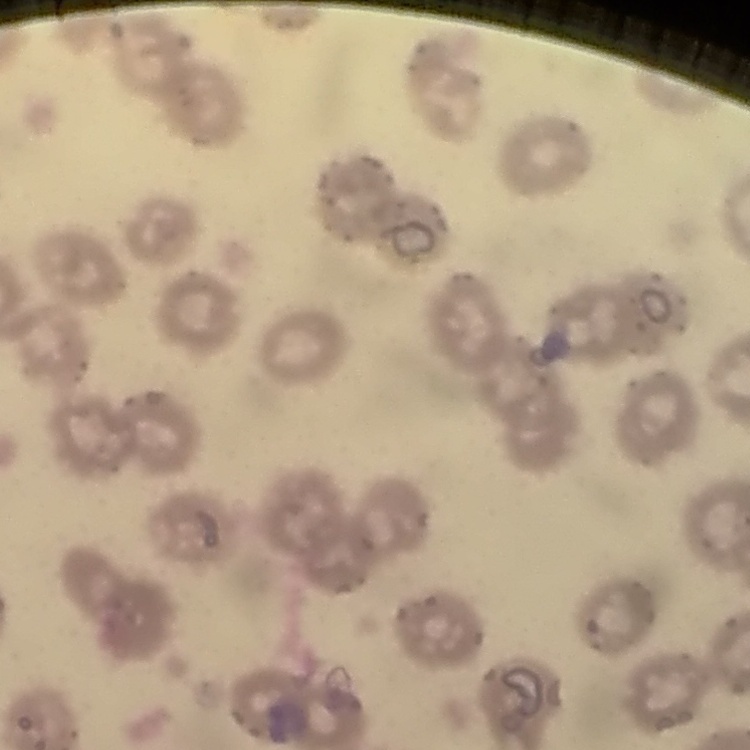 The erythrocytes show no rouleaux formation. Thin blood smear. Square crop of a larger photomicrograph. Stained with either Field's or Giemsa.